Classify this cell by malaria status.
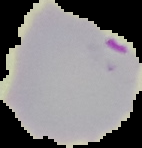

It is parasitized.

The area outside the segmented cell region is set to black. Image is 142×148 pixels. From a thin blood smear.